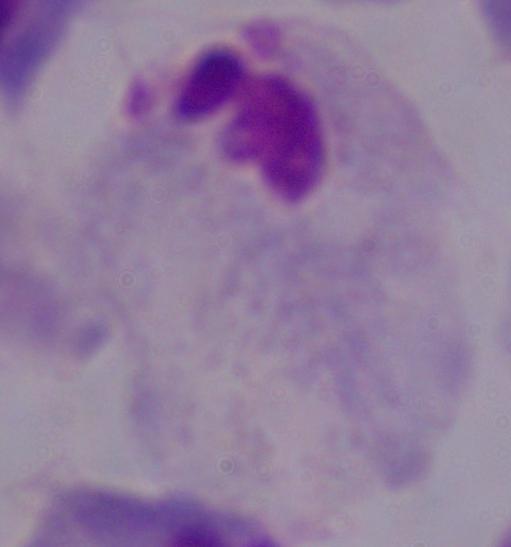

modality = micrograph
magnification = 1000x
identification = trichomonad